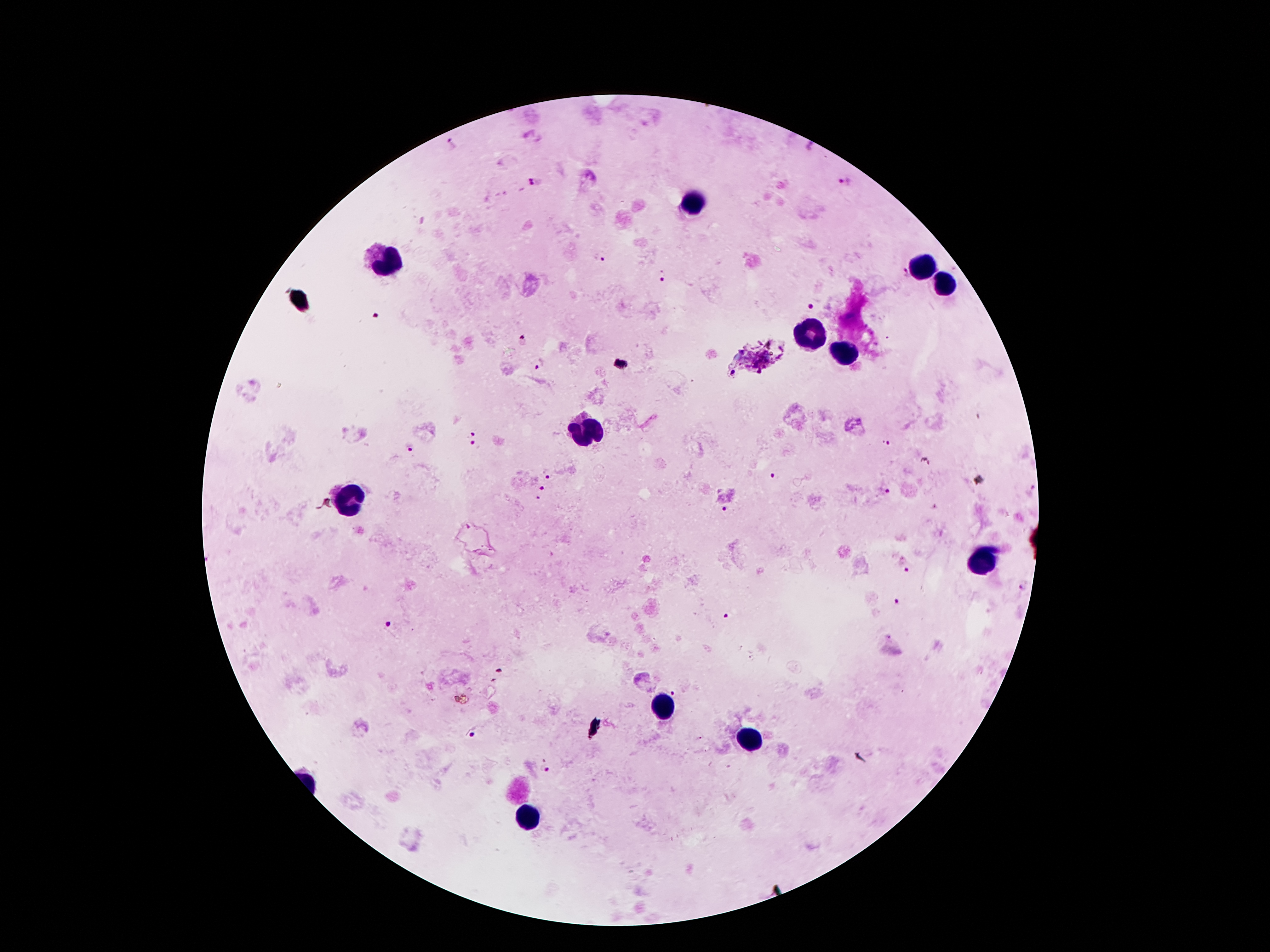

Approximate centers as {x, y} in pixels.
Summary:
  - Plasmodium parasite locations: {846, 181}, {534, 183}, {600, 256}, {900, 273}, {661, 276}, {807, 307}, {375, 316}, {521, 341}, {537, 364}, {469, 434}, {886, 444}, {473, 447}, {409, 449}, {550, 476}, {772, 476}, {1033, 487}, {541, 490}, {886, 492}, {540, 500}, {726, 512}, {908, 572}, {1022, 586}, {896, 604}, {727, 619}, {391, 625}, {500, 670}, {676, 692}, {473, 736}, {545, 769}
  - Leukocyte locations: {690, 201}, {387, 261}, {925, 267}, {941, 286}, {810, 336}, {844, 357}, {590, 428}, {351, 498}, {975, 564}, {660, 707}, {749, 741}, {528, 822}
  - Magnification: 100x
  - Patient malaria status: infected with Plasmodium falciparum
  - Preparation: thick peripheral-blood smear
  - Stain: Giemsa
  - Field of view: single
  - Image size: 1270×952 pixels
  - Capture: smartphone through the microscope eyepiece